Locate every blood parasite and identify its species.
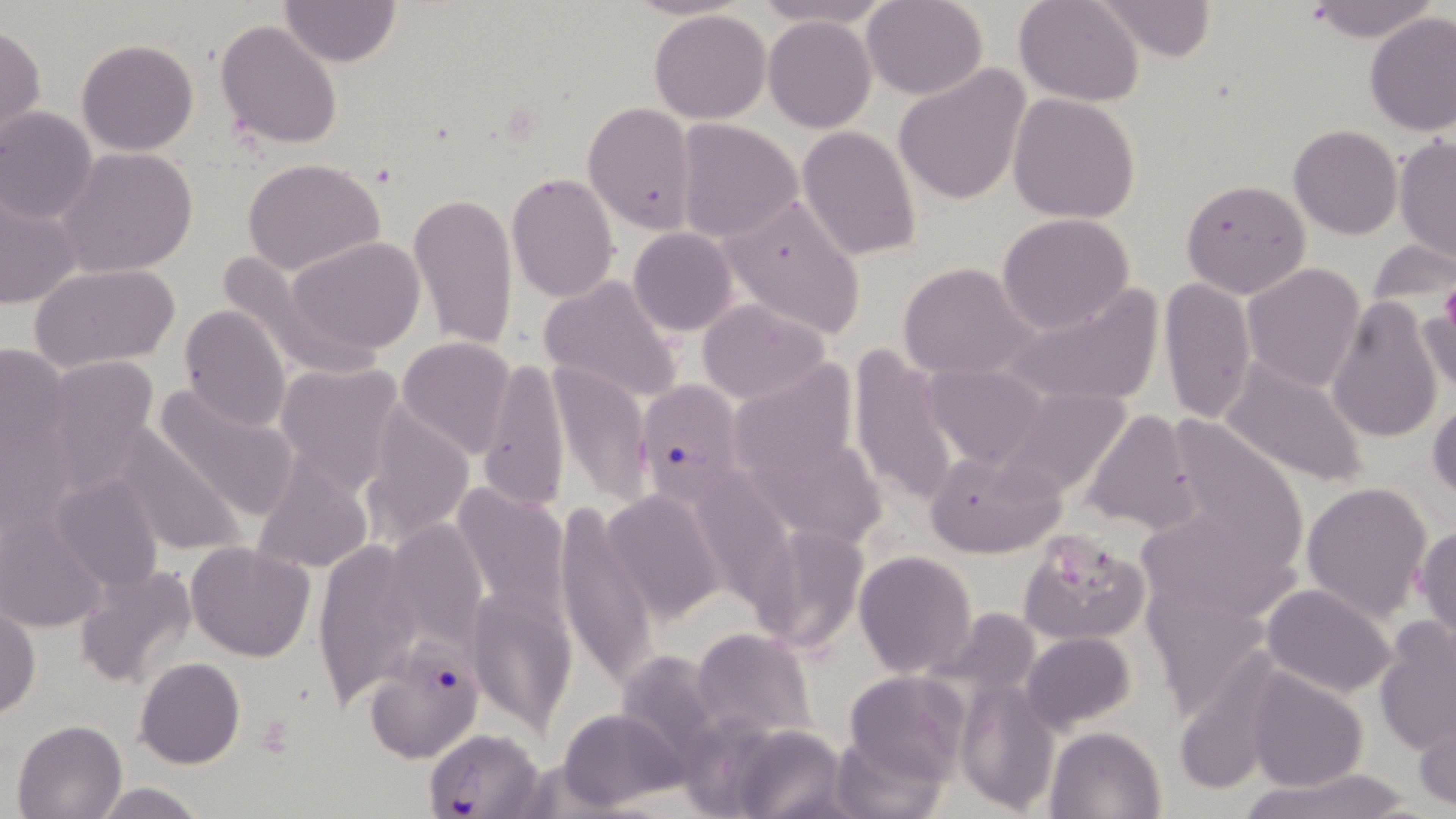

Approximate bounding boxes as (x1, y1, x2, y2) in pixels.
Plasmodium falciparum-infected red blood cells: (632, 377, 749, 503), (365, 649, 483, 765), (424, 727, 546, 819).
No Plasmodium ovale, Plasmodium malariae, Plasmodium vivax, Babesia divergens, or Trypanosoma brucei observed.

slide-level diagnosis = Plasmodium falciparum
field of view = single
preparation = thin blood smear
modality = optical microscopy
stain = May-Grünwald-Giemsa
platelet locations = approximate bounding boxes as (x1, y1, x2, y2) in pixels: (1441, 281, 1456, 336), (1047, 541, 1114, 597)
uninfected red blood cell locations = approximate bounding boxes as (x1, y1, x2, y2) in pixels: (278, 0, 401, 67), (754, 0, 892, 30), (861, 0, 988, 99), (1013, 0, 1145, 106), (1097, 0, 1217, 64), (1308, 0, 1432, 43), (649, 9, 773, 124), (1364, 11, 1456, 134), (763, 16, 878, 132), (214, 19, 343, 152), (1, 25, 46, 148), (77, 38, 198, 155), (892, 64, 1032, 206), (1007, 92, 1141, 224), (582, 102, 698, 234), (0, 106, 97, 225), (673, 118, 803, 241), (796, 125, 921, 260), (1288, 125, 1401, 240), (1394, 136, 1455, 265), (56, 146, 199, 278), (244, 159, 386, 275), (505, 171, 620, 305), (1179, 177, 1312, 299), (0, 188, 83, 311), (407, 193, 520, 352), (718, 194, 867, 340), (996, 213, 1136, 332), (627, 227, 739, 336), (285, 237, 427, 356), (1367, 238, 1453, 314), (212, 247, 378, 381), (1241, 261, 1366, 392), (898, 262, 1041, 381), (29, 263, 182, 373), (538, 273, 686, 404), (1157, 276, 1258, 423), (1000, 285, 1165, 411), (1327, 294, 1444, 444), (1416, 296, 1456, 405), (695, 298, 833, 406), (178, 303, 292, 431), (397, 337, 518, 459), (0, 341, 74, 490), (847, 345, 965, 507), (747, 354, 869, 467), (38, 355, 162, 488), (478, 357, 569, 512), (1220, 357, 1372, 488), (273, 360, 408, 497), (550, 361, 651, 508), (920, 363, 1053, 472), (149, 382, 301, 521), (992, 385, 1135, 501), (1427, 394, 1456, 504), (359, 403, 475, 545), (1081, 408, 1201, 533), (110, 426, 246, 557), (759, 444, 900, 552), (924, 449, 1067, 559), (252, 461, 375, 575), (48, 469, 166, 598), (451, 481, 571, 618), (1301, 482, 1433, 622), (601, 489, 725, 621), (701, 495, 814, 639), (555, 504, 656, 691), (1135, 507, 1292, 620), (385, 519, 486, 648), (1413, 522, 1456, 650), (749, 523, 869, 658), (1018, 528, 1152, 646), (313, 539, 427, 705), (185, 541, 315, 662), (853, 551, 977, 679), (73, 564, 199, 693), (1142, 581, 1276, 720), (1261, 582, 1396, 699), (466, 587, 575, 730), (0, 602, 41, 720), (936, 606, 1048, 715), (1373, 619, 1455, 755), (690, 628, 815, 740), (1021, 631, 1136, 731), (618, 646, 744, 757), (135, 657, 245, 770), (1244, 670, 1368, 792), (843, 671, 969, 785), (957, 683, 1061, 814), (558, 706, 687, 811), (1413, 709, 1456, 812), (11, 718, 128, 819), (1045, 725, 1167, 818), (736, 726, 852, 818), (829, 731, 946, 818), (1240, 769, 1421, 819), (93, 781, 209, 819)
image size = 1456×819 pixels
magnification = 1000x